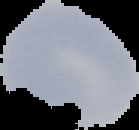

Summary:
  - Preparation: thin blood smear
  - Image type: segmented cell region on a black background
  - Result: negative for malaria parasites
  - Image size: 139×130 pixels